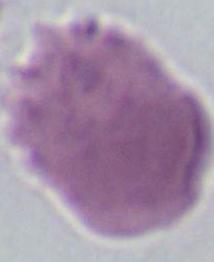

Summary:
  - Identification: erythrocyte
  - Modality: photomicrograph
  - Magnification: 1000x